State which parasite is depicted.
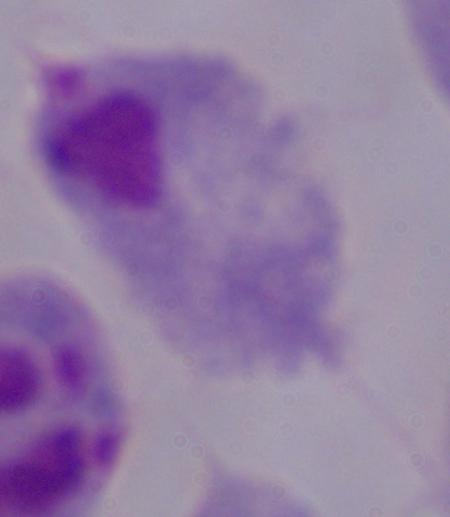
A trichomonad.

Micrograph. Captured at 1000x magnification.